Identify the parasite.
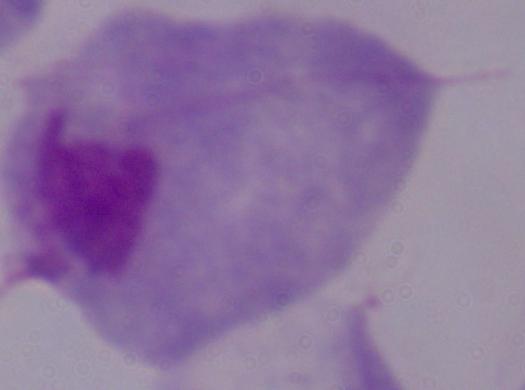

A trichomonad.

Photomicrograph. Captured at 1000x magnification.